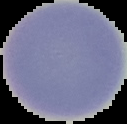
From a thin blood film. Image is 127×124 pixels. Segmented cell region on a black background. Malaria status: uninfected.